Comment on the morphology of the red blood cells.
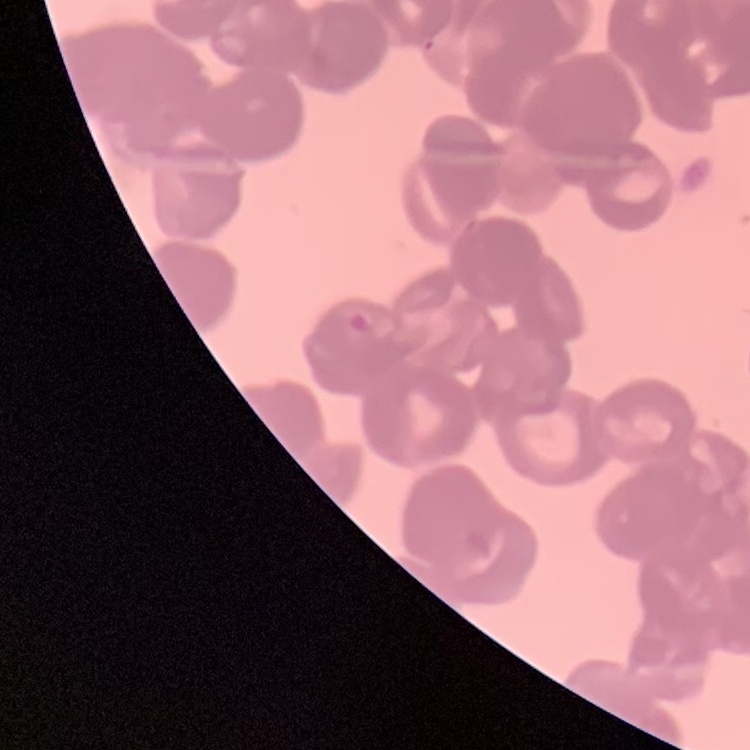

Rouleaux formation.

preparation: thin peripheral smear
image_type: one tile cut from a larger photomicrograph
stain: Field's or Giemsa